Report the malaria status of this cell.
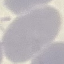

Uninfected.

Giemsa-stained preparation. Acquired by smartphone through the microscope eyepiece. Thin blood smear. Cell patch, automatically extracted from a larger field of view and resized to 64 × 64 pixels.